State which parasite is depicted.
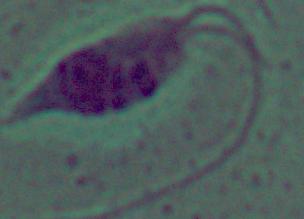

This is Leishmania.

Summary:
  - Magnification: 1000x
  - Modality: micrograph